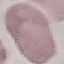

Summary:
  - Malaria status: uninfected
  - Stain: Giemsa
  - Capture: smartphone camera at the microscope eyepiece
  - Image type: automatically extracted cell patch, resized to 64 × 64 pixels
  - Preparation: thin blood smear